Report the malaria status.
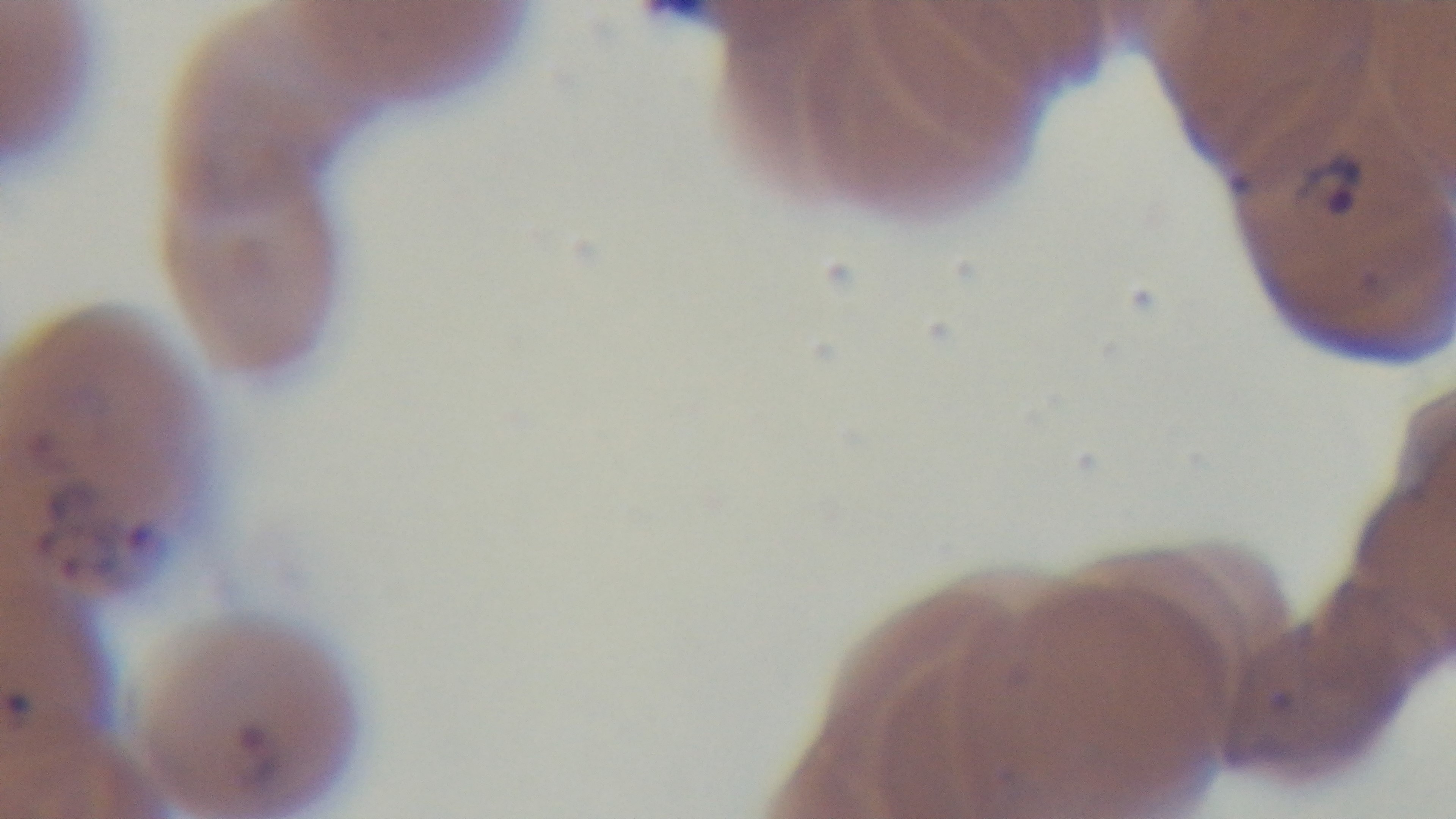

Positive.

Photomicrograph. Oil-immersion objective, 100x. Captured with a mounted 4K digital camera. Giemsa-stained. One field from the slide. Preparation: thin.